Find the cells and give the type of each one.
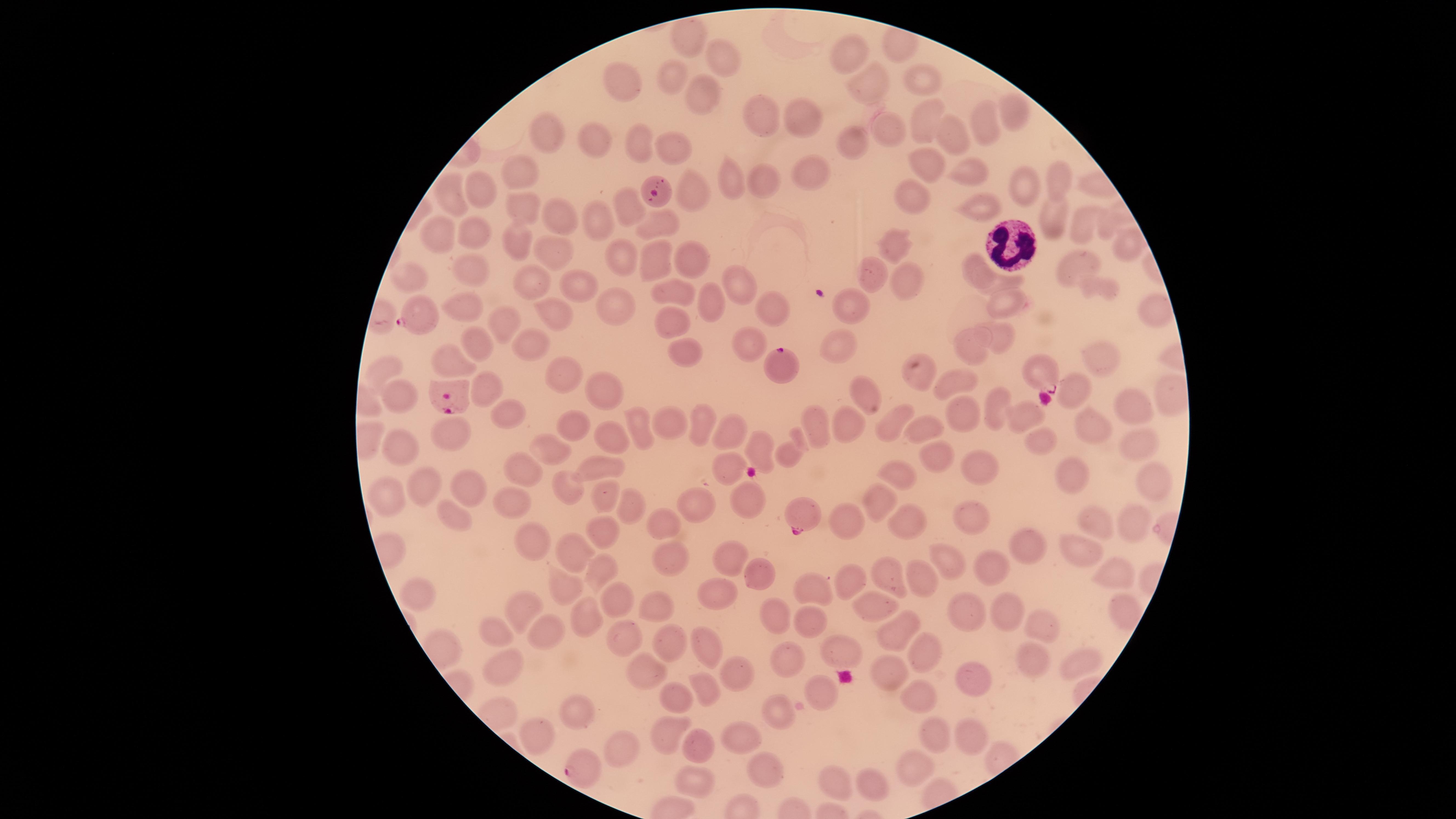
Approximate marker points as {x, y} in pixels.
Parasitized red blood cells: {421, 314}, {779, 362}, {1042, 372}, {451, 397}, {803, 514}, {580, 769}.
Uninfected red blood cells: {684, 32}, {851, 56}, {723, 57}, {615, 79}, {671, 79}, {925, 83}, {865, 84}, {698, 93}, {1019, 113}, {762, 120}, {800, 120}, {921, 120}, {985, 120}, {890, 130}, {546, 133}, {959, 134}, {593, 142}, {641, 144}, {677, 145}, {848, 145}, {924, 163}, {806, 171}, {963, 172}, {521, 176}, {1064, 178}, {765, 180}, {735, 183}, {1033, 187}, {482, 188}, {690, 192}, {910, 194}, {448, 195}, {520, 204}, {622, 205}, {982, 207}, {556, 217}, {1051, 218}, {594, 219}, {1078, 224}, {664, 225}, {473, 234}, {437, 235}, {515, 243}, {894, 246}, {1127, 247}, {552, 249}, {624, 254}, {656, 255}, {691, 258}, {1074, 262}, {977, 267}, {474, 271}, {875, 273}, {404, 278}, {532, 279}, {1008, 279}, {903, 282}, {574, 285}, {737, 287}, {1094, 287}, {674, 289}, {706, 303}, {464, 304}, {846, 304}, {1002, 304}, {617, 310}, {1147, 310}, {772, 311}, {553, 312}, {672, 318}, {504, 321}, {996, 337}, {837, 341}, {974, 342}, {533, 344}, {478, 346}, {749, 348}, {684, 353}, {1102, 360}, {455, 361}, {385, 365}, {552, 370}, {919, 371}, {481, 379}, {954, 381}, {1077, 386}, {605, 390}, {1167, 390}, {865, 392}, {394, 399}, {994, 403}, {1134, 407}, {963, 411}, {509, 412}, {1022, 413}, {665, 419}, {704, 419}, {849, 422}, {566, 423}, {814, 423}, {890, 423}, {1095, 426}, {641, 427}, {728, 427}, {922, 429}, {456, 434}, {618, 440}, {1040, 442}, {758, 444}, {1140, 444}, {397, 448}, {555, 453}, {785, 453}, {937, 455}, {521, 464}, {602, 465}, {730, 465}, {982, 467}, {888, 471}, {1075, 474}, {1151, 477}, {432, 485}, {478, 485}, {570, 485}, {602, 496}, {392, 500}, {630, 500}, {511, 501}, {699, 501}, {747, 501}, {871, 505}, {455, 511}, {967, 512}, {845, 516}, {669, 521}, {906, 524}, {1096, 525}, {1133, 525}, {600, 530}, {528, 541}, {1027, 543}, {574, 550}, {1083, 552}, {731, 558}, {667, 559}, {948, 563}, {992, 566}, {601, 573}, {844, 575}, {1112, 575}, {889, 576}, {765, 577}, {922, 580}, {567, 585}, {813, 585}, {722, 595}, {417, 596}, {615, 600}, {650, 600}, {866, 604}, {968, 606}, {526, 608}, {1122, 608}, {1008, 614}, {583, 615}, {776, 617}, {547, 623}, {808, 623}, {1038, 626}, {494, 629}, {893, 629}, {618, 632}, {673, 639}, {704, 641}, {921, 646}, {837, 652}, {1038, 659}, {787, 662}, {1077, 662}, {498, 666}, {636, 669}, {732, 675}, {891, 676}, {970, 677}, {707, 688}, {818, 689}, {680, 694}, {915, 695}, {579, 708}, {782, 710}, {669, 729}, {937, 734}, {536, 736}, {732, 737}, {966, 738}, {698, 745}, {612, 747}, {909, 762}, {760, 767}, {831, 778}, {690, 779}, {862, 784}.
White blood cells: {1009, 244}.

Smartphone photograph through the microscope eyepiece. Single field of view. Thin blood smear. Circular visible region. Image is 1456×819 pixels. Species: Plasmodium falciparum. Giemsa-stained preparation.